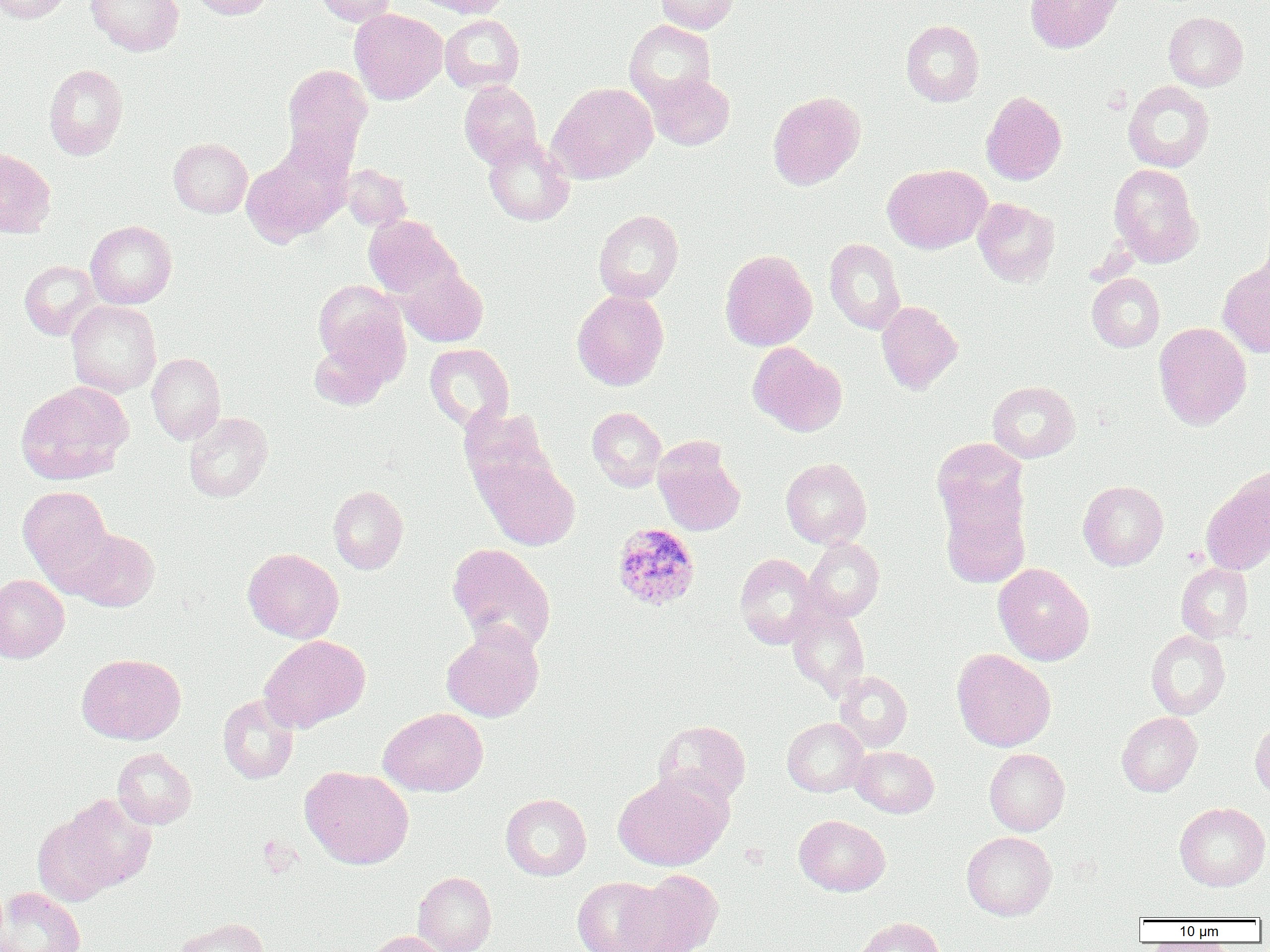
Plasmodium ovale-infected red blood cell locations = approximate bounding boxes as named x1/y1/x2/y2 corners in pixels: (x1=611, y1=523, x2=700, y2=610)
slide-level diagnosis = Plasmodium ovale
magnification = 1000x
modality = light microscopy
field of view = single
uninfected red blood cell locations = approximate bounding boxes as named x1/y1/x2/y2 corners in pixels: (x1=0, y1=0, x2=72, y2=23), (x1=86, y1=0, x2=184, y2=56), (x1=189, y1=0, x2=274, y2=19), (x1=314, y1=0, x2=397, y2=26), (x1=415, y1=0, x2=509, y2=18), (x1=656, y1=0, x2=739, y2=34), (x1=1025, y1=0, x2=1123, y2=52), (x1=350, y1=9, x2=447, y2=104), (x1=1164, y1=12, x2=1248, y2=91), (x1=440, y1=15, x2=524, y2=93), (x1=624, y1=20, x2=716, y2=108), (x1=901, y1=20, x2=984, y2=106), (x1=43, y1=64, x2=128, y2=160), (x1=282, y1=64, x2=372, y2=162), (x1=645, y1=72, x2=734, y2=150), (x1=459, y1=81, x2=542, y2=168), (x1=1123, y1=81, x2=1214, y2=172), (x1=548, y1=82, x2=657, y2=184), (x1=981, y1=91, x2=1067, y2=185), (x1=767, y1=92, x2=865, y2=190), (x1=483, y1=133, x2=574, y2=226), (x1=169, y1=138, x2=252, y2=217), (x1=240, y1=145, x2=350, y2=244), (x1=0, y1=148, x2=56, y2=238), (x1=341, y1=164, x2=412, y2=231), (x1=882, y1=164, x2=991, y2=253), (x1=1109, y1=164, x2=1204, y2=266), (x1=973, y1=198, x2=1059, y2=286), (x1=593, y1=209, x2=684, y2=303), (x1=363, y1=215, x2=459, y2=300), (x1=85, y1=220, x2=177, y2=309), (x1=825, y1=238, x2=905, y2=334), (x1=719, y1=249, x2=817, y2=351), (x1=20, y1=260, x2=100, y2=340), (x1=1218, y1=261, x2=1270, y2=357), (x1=399, y1=266, x2=488, y2=347), (x1=1087, y1=273, x2=1165, y2=352), (x1=312, y1=280, x2=407, y2=371), (x1=572, y1=289, x2=670, y2=390), (x1=66, y1=300, x2=161, y2=397), (x1=877, y1=301, x2=962, y2=394), (x1=1154, y1=322, x2=1252, y2=430), (x1=309, y1=336, x2=394, y2=409), (x1=748, y1=342, x2=847, y2=436), (x1=424, y1=343, x2=515, y2=432), (x1=147, y1=352, x2=225, y2=444), (x1=16, y1=381, x2=133, y2=485), (x1=988, y1=381, x2=1080, y2=462), (x1=459, y1=406, x2=557, y2=506), (x1=587, y1=406, x2=667, y2=492), (x1=184, y1=412, x2=273, y2=502), (x1=931, y1=437, x2=1029, y2=537), (x1=653, y1=438, x2=746, y2=535), (x1=479, y1=456, x2=581, y2=551), (x1=780, y1=458, x2=871, y2=548), (x1=1201, y1=471, x2=1270, y2=573), (x1=1078, y1=480, x2=1168, y2=570), (x1=17, y1=485, x2=114, y2=587), (x1=328, y1=485, x2=408, y2=574), (x1=939, y1=488, x2=1031, y2=588), (x1=66, y1=528, x2=160, y2=612), (x1=801, y1=537, x2=884, y2=623), (x1=447, y1=543, x2=556, y2=654), (x1=243, y1=548, x2=344, y2=643), (x1=735, y1=553, x2=820, y2=648), (x1=993, y1=563, x2=1094, y2=665), (x1=1176, y1=563, x2=1253, y2=642), (x1=0, y1=574, x2=69, y2=662), (x1=786, y1=605, x2=869, y2=700), (x1=441, y1=624, x2=544, y2=722), (x1=1146, y1=629, x2=1230, y2=720), (x1=259, y1=634, x2=370, y2=732), (x1=951, y1=649, x2=1055, y2=751), (x1=76, y1=653, x2=186, y2=745), (x1=835, y1=671, x2=912, y2=752), (x1=218, y1=694, x2=299, y2=784), (x1=378, y1=707, x2=488, y2=796), (x1=1117, y1=712, x2=1202, y2=796), (x1=782, y1=717, x2=868, y2=797), (x1=1250, y1=717, x2=1270, y2=800), (x1=653, y1=720, x2=751, y2=807), (x1=851, y1=746, x2=939, y2=817), (x1=112, y1=748, x2=196, y2=829), (x1=984, y1=748, x2=1070, y2=836), (x1=300, y1=766, x2=414, y2=869), (x1=613, y1=772, x2=731, y2=871), (x1=45, y1=793, x2=157, y2=898), (x1=501, y1=793, x2=591, y2=880), (x1=1174, y1=802, x2=1269, y2=891), (x1=794, y1=815, x2=890, y2=896), (x1=961, y1=831, x2=1057, y2=920), (x1=619, y1=870, x2=723, y2=952), (x1=413, y1=871, x2=497, y2=952), (x1=572, y1=876, x2=668, y2=952), (x1=0, y1=887, x2=86, y2=952), (x1=176, y1=917, x2=271, y2=952), (x1=853, y1=917, x2=946, y2=952), (x1=368, y1=931, x2=451, y2=952)
preparation = thin blood smear
image size = 1270×952 pixels